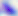
modality: photomicrograph
identification: Toxoplasma gondii
magnification: 400x